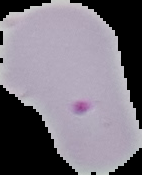
image size = 142×175 pixels
image type = cell region segmented out of the field of view; surrounding area masked to black
result = malaria parasites identified
preparation = thin blood film